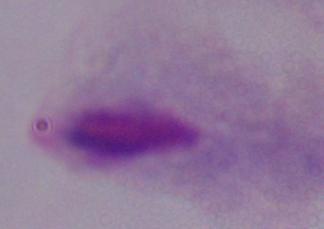
identification: trichomonad
magnification: 1000x
modality: micrograph